Comment on the morphology of the erythrocytes.
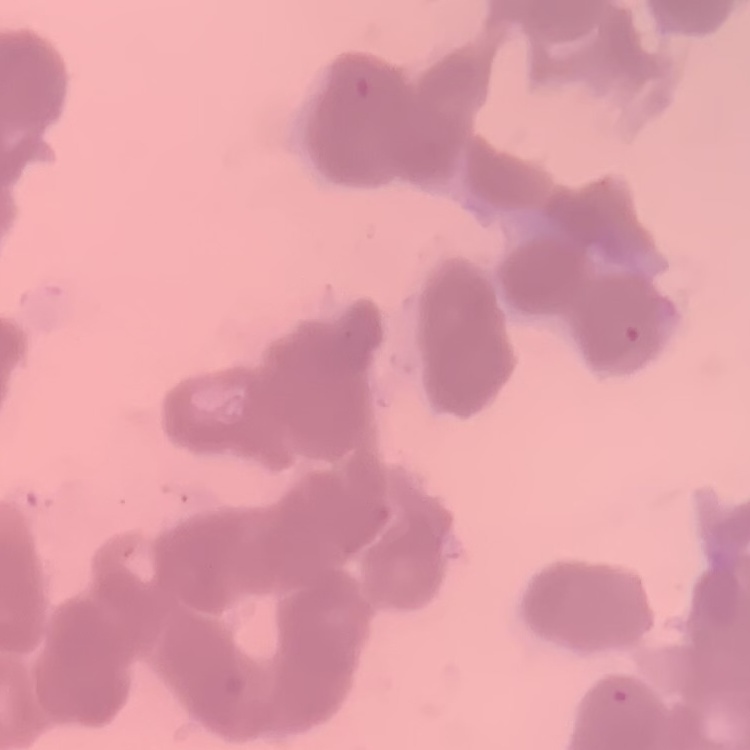

They show rouleaux formation.

image type = one tile cut from a larger photomicrograph
stain = Field's or Giemsa
preparation = thin blood smear